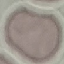
{
  "malaria_status": "uninfected",
  "preparation": "thin smear",
  "capture": "smartphone through the microscope eyepiece",
  "image_type": "automatically extracted cell patch, resized to 64 × 64 pixels",
  "stain": "Giemsa"
}